Assess this cell for malaria.
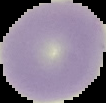
Uninfected.

Image is 106×103 pixels. The area outside the segmented cell region is set to black. From a thin blood film.